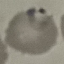
Malaria status: parasitized. Cell patch, automatically extracted from a larger field of view and resized to 64 × 64 pixels. Acquired by smartphone through the microscope eyepiece. Thin blood film. Giemsa stain.